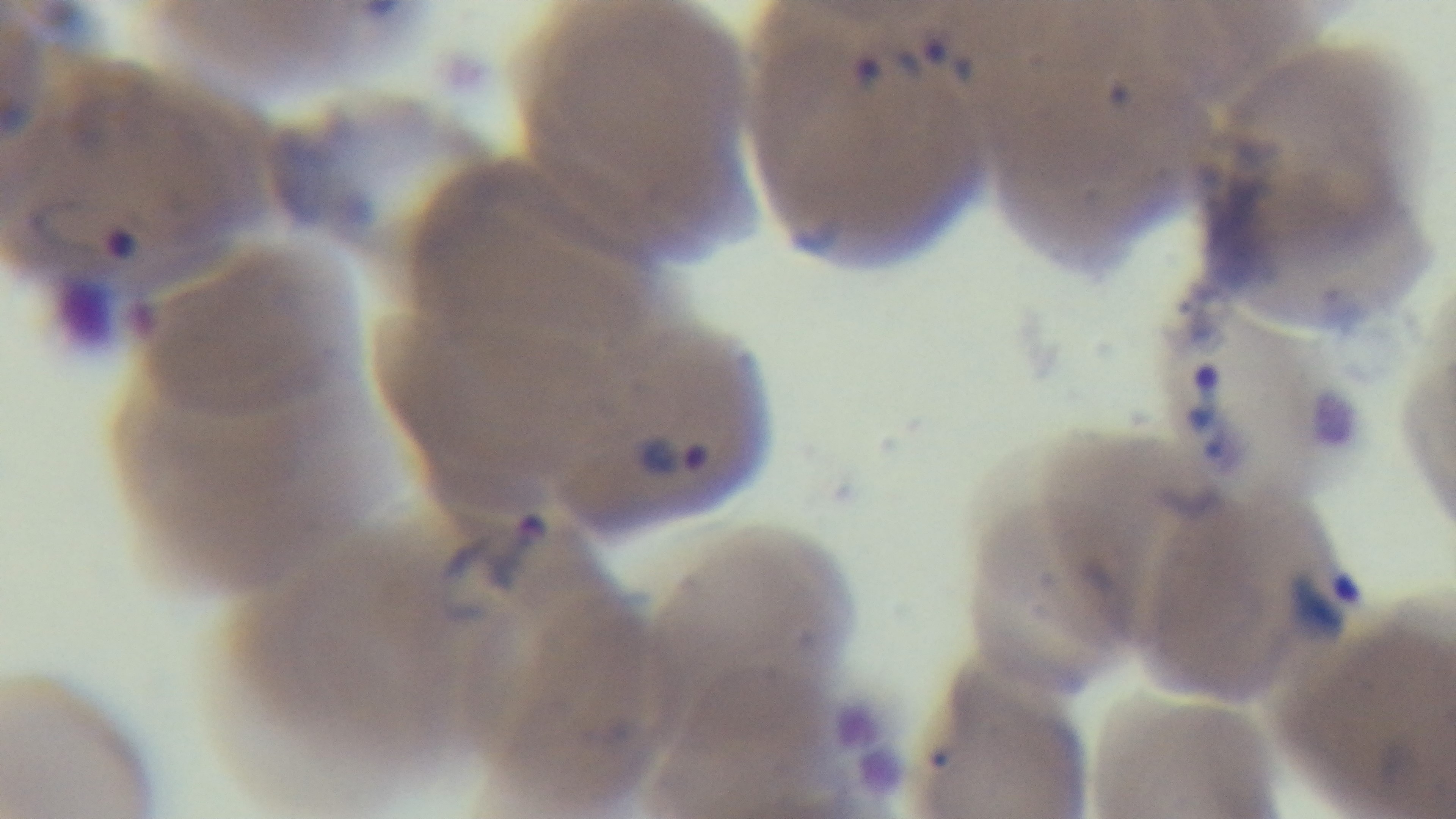

Summary:
  - Field of view: one from the slide
  - Preparation: thin
  - Capture: mounted 4K digital camera
  - Modality: light microscopy
  - Stain: Giemsa
  - Objective: 100x oil immersion
  - Malaria status: positive